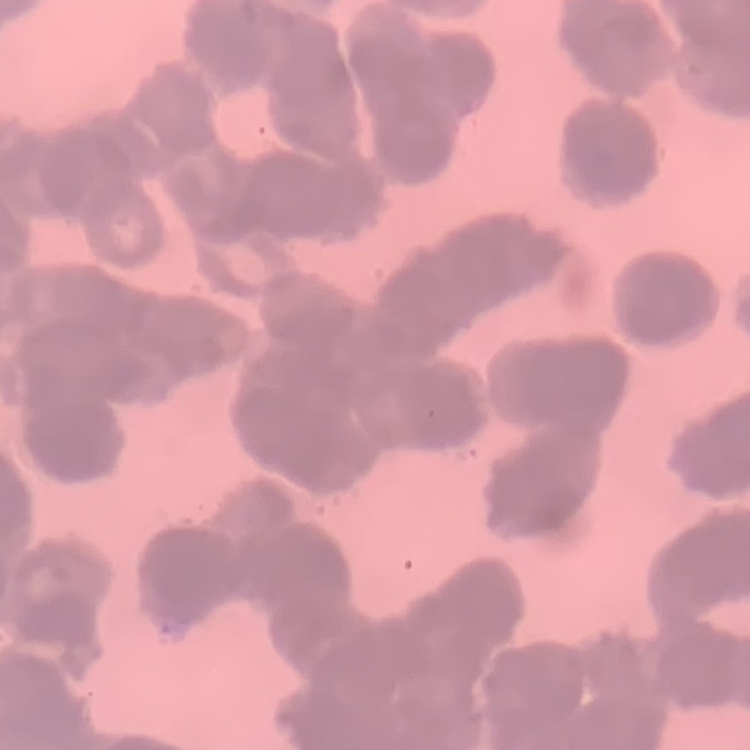

Summary:
  - Erythrocyte morphology: rouleaux formation
  - Stain: Field's or Giemsa
  - Image type: square crop of a larger photomicrograph
  - Preparation: thin blood film